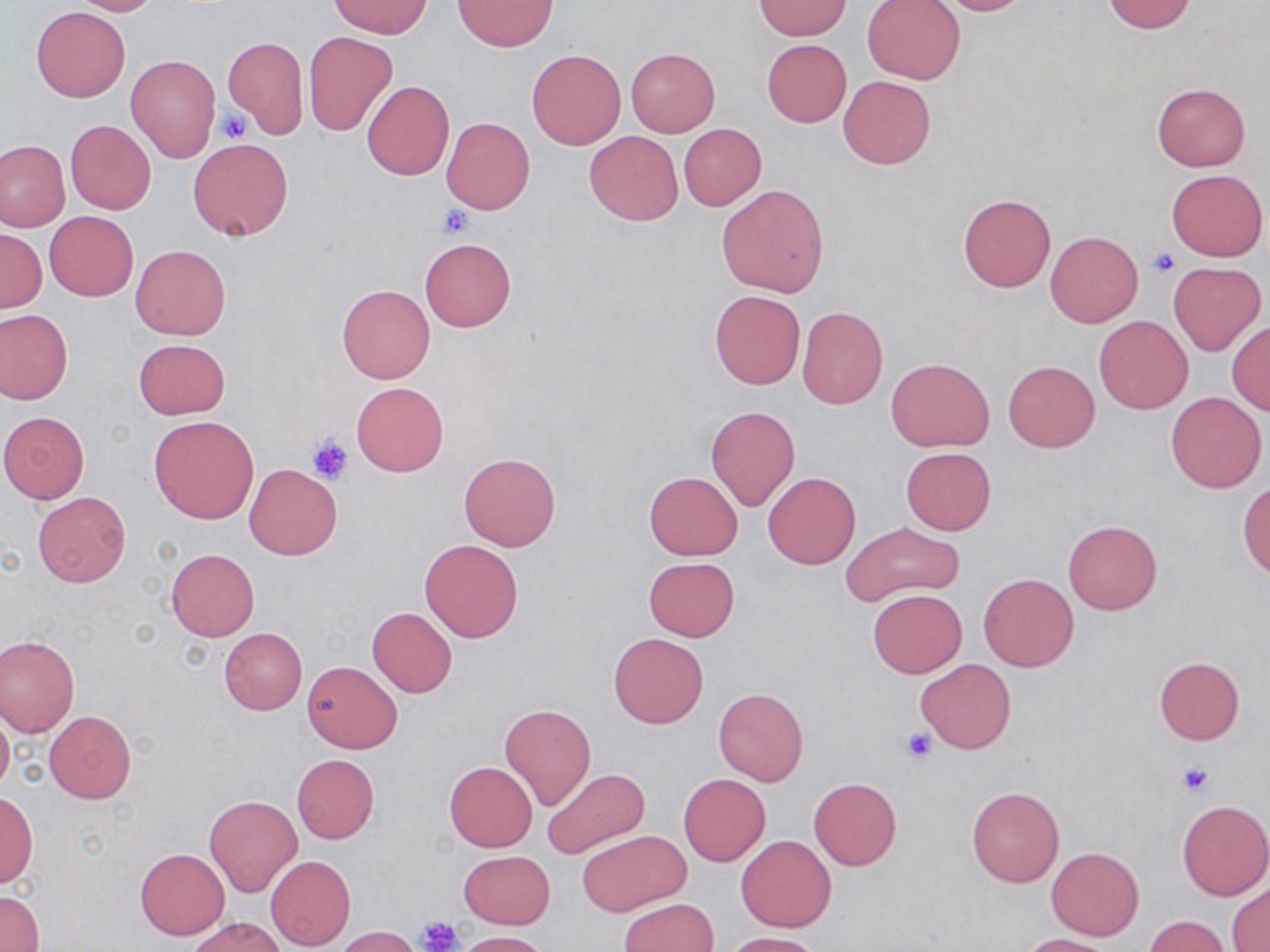
Summary:
  - Coordinate format: approximate bounding boxes as [x1, y1, x2, y2] in pixels
  - Uninfected red blood cell locations: [69, 0, 162, 16], [927, 0, 1033, 15], [331, 1, 431, 38], [452, 1, 556, 51], [756, 1, 849, 39], [861, 1, 965, 84], [1101, 1, 1196, 34], [31, 6, 130, 102], [304, 31, 397, 136], [222, 37, 309, 138], [762, 39, 851, 127], [526, 48, 625, 149], [625, 48, 720, 135], [126, 55, 220, 162], [837, 75, 936, 170], [361, 81, 455, 181], [1152, 82, 1251, 171], [442, 117, 535, 214], [65, 119, 157, 215], [678, 123, 766, 210], [584, 130, 683, 225], [188, 138, 293, 240], [0, 140, 70, 231], [1165, 168, 1267, 261], [716, 184, 829, 297], [956, 193, 1056, 292], [44, 211, 139, 302], [1, 230, 46, 313], [1044, 231, 1143, 328], [419, 238, 517, 332], [131, 244, 230, 340], [1170, 261, 1266, 354], [337, 284, 434, 383], [709, 289, 806, 390], [796, 306, 890, 409], [0, 309, 72, 403], [1094, 316, 1192, 414], [1227, 322, 1270, 415], [133, 339, 230, 420], [886, 358, 993, 452], [1004, 361, 1098, 452], [352, 382, 448, 476], [1165, 392, 1266, 492], [706, 405, 799, 510], [0, 411, 90, 503], [149, 416, 258, 524], [900, 448, 995, 534], [458, 454, 561, 552], [244, 463, 342, 560], [643, 471, 743, 559], [763, 471, 860, 569], [1238, 482, 1270, 577], [33, 492, 130, 586], [1062, 520, 1162, 614], [842, 521, 966, 610], [419, 539, 524, 642], [166, 548, 258, 641], [643, 557, 741, 641], [978, 572, 1078, 671], [867, 588, 967, 677], [368, 607, 457, 698], [219, 628, 307, 714], [608, 633, 709, 729], [0, 634, 80, 738], [1154, 657, 1244, 744], [917, 658, 1015, 754], [302, 660, 401, 753], [713, 687, 809, 786], [499, 704, 596, 810], [0, 706, 14, 795], [43, 711, 137, 803], [291, 754, 379, 843], [444, 761, 537, 851], [541, 768, 649, 858], [679, 774, 770, 866], [808, 777, 902, 869], [966, 786, 1063, 887], [1, 789, 36, 889], [204, 793, 302, 897], [1176, 801, 1270, 901], [577, 830, 689, 916], [736, 835, 835, 932], [1046, 846, 1144, 939], [135, 848, 230, 939], [459, 851, 553, 929], [266, 855, 355, 951], [1228, 883, 1270, 952], [0, 891, 44, 952], [618, 898, 717, 952], [1142, 915, 1229, 951], [188, 916, 281, 952], [333, 926, 424, 951], [454, 930, 551, 952], [722, 932, 822, 952], [1021, 934, 1117, 952]
  - Platelet locations: [217, 106, 251, 143], [437, 204, 473, 238], [1147, 250, 1178, 277], [306, 432, 354, 484], [898, 726, 937, 764], [1177, 762, 1213, 796], [420, 915, 464, 952]
  - Slide-level diagnosis: no evidence of blood parasites
  - Stain: May-Grünwald-Giemsa
  - Field of view: one of a larger specimen
  - Magnification: 1000x
  - Modality: light microscopy
  - Preparation: thin blood film
  - Image size: 1270×952 pixels